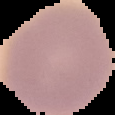
preparation: thin blood smear
image_size: 115×115 pixels
image_type: segmented cell region with the area outside set to black
malaria_status: uninfected